Evaluate for malaria.
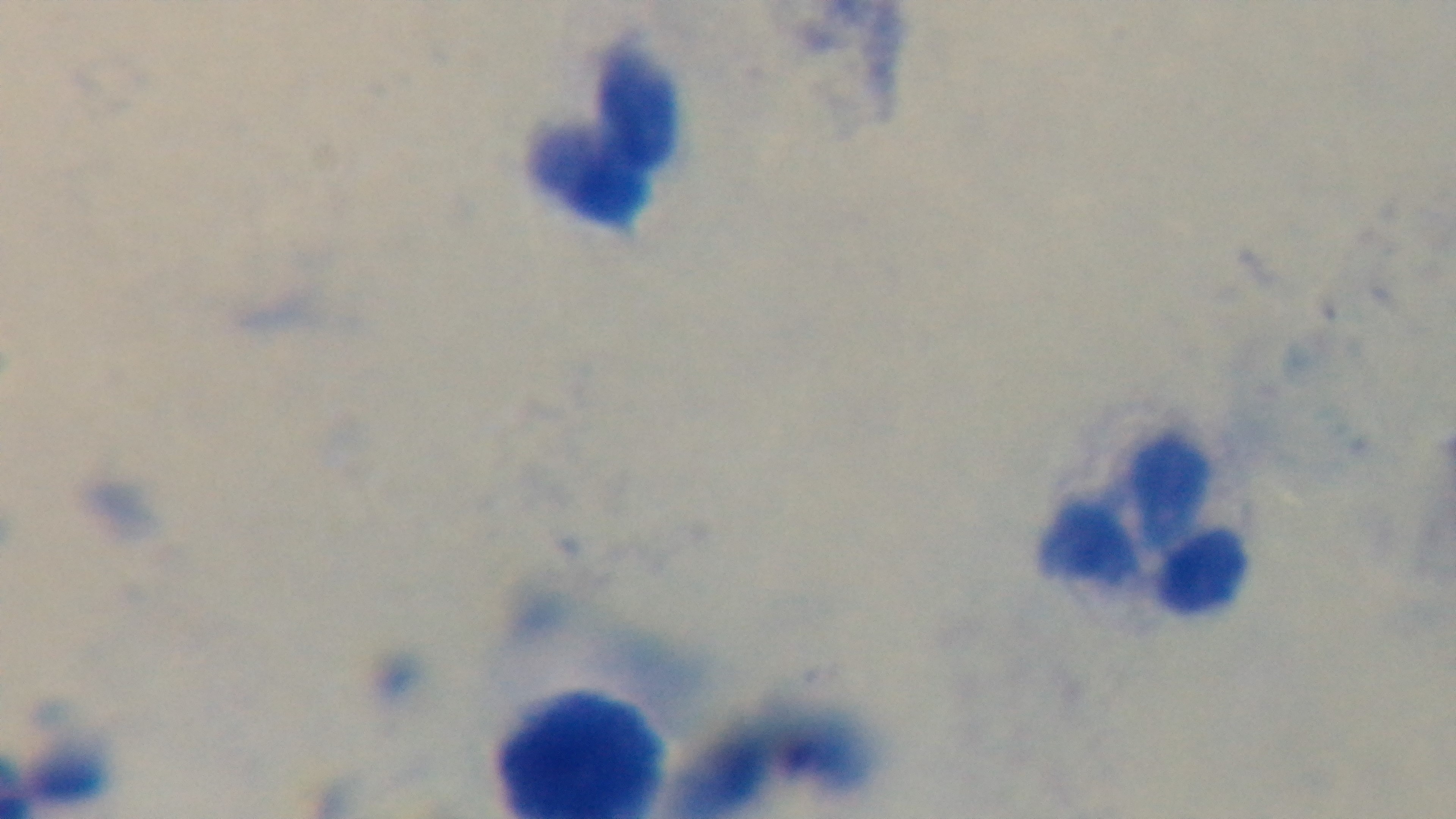
It is uninfected.

100x oil-immersion objective. Giemsa stain. Captured with a mounted 4K digital camera. Preparation: thick smear. Light microscopy. One field from the slide.